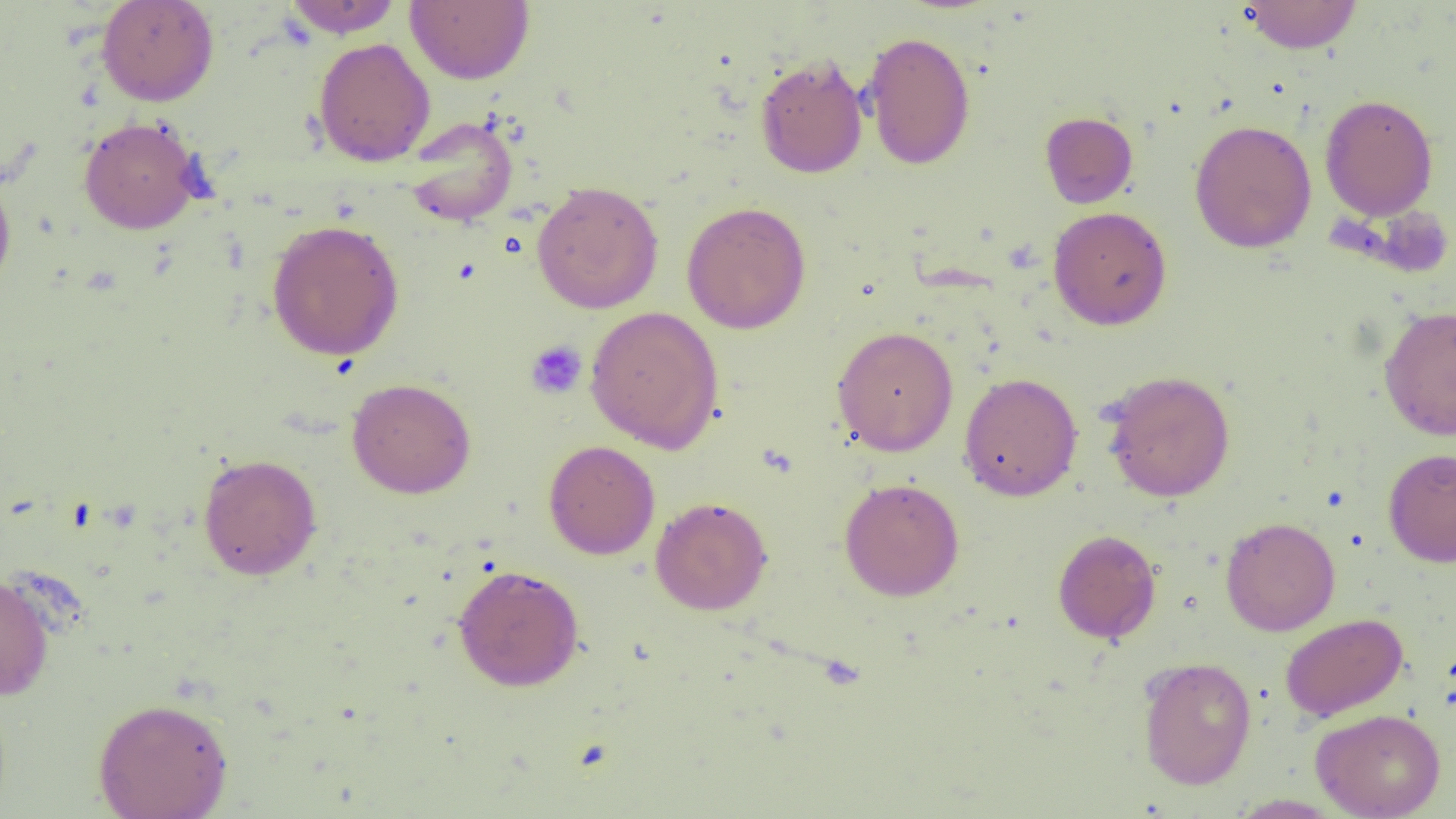
slide-level diagnosis = negative for blood parasites
magnification = 1000x
platelet locations = approximate bounding boxes as (x1, y1, x2, y2) in pixels: (525, 340, 588, 399)
preparation = thin blood smear
image size = 1456×819 pixels
uninfected red blood cell locations = approximate bounding boxes as (x1, y1, x2, y2) in pixels: (96, 0, 219, 106), (283, 0, 403, 38), (405, 0, 535, 85), (1239, 0, 1363, 54), (862, 31, 976, 170), (313, 37, 435, 166), (754, 54, 868, 178), (1319, 94, 1439, 220), (1040, 111, 1138, 209), (78, 116, 203, 234), (403, 116, 518, 227), (1189, 119, 1317, 253), (0, 170, 17, 299), (531, 180, 663, 314), (681, 202, 811, 334), (1048, 206, 1172, 330), (266, 219, 405, 361), (1378, 304, 1456, 440), (585, 305, 724, 453), (832, 326, 959, 456), (1101, 370, 1236, 502), (959, 371, 1083, 502), (346, 377, 476, 498), (544, 440, 660, 559), (1383, 447, 1456, 567), (197, 453, 322, 580), (839, 477, 965, 601), (650, 496, 772, 615), (1220, 517, 1340, 636), (1052, 528, 1161, 644), (452, 564, 584, 691), (0, 572, 55, 702), (1280, 613, 1408, 721), (1138, 656, 1257, 789), (92, 697, 233, 819), (1311, 708, 1446, 819), (1226, 794, 1345, 818)
field of view = single
modality = optical microscopy